State the preparation type.
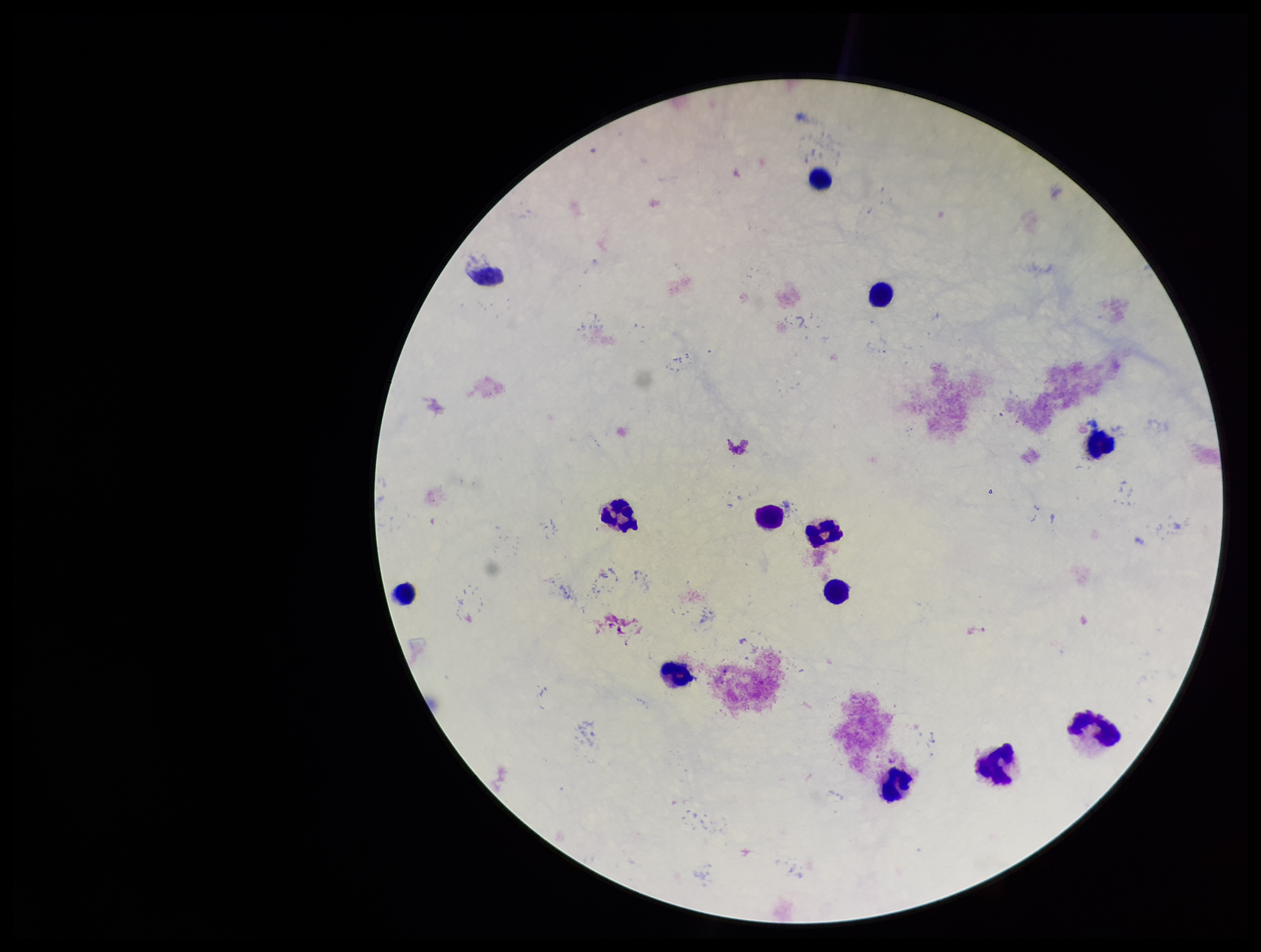
It is a thick blood smear.

Summary:
  - Image size: 1261×952 pixels
  - Field of view: single
  - Leukocyte count: 12
  - Stain: Giemsa
  - Parasite count: 0
  - Capture: smartphone photograph through the microscope eyepiece
  - Plasmodium parasites: none seen
  - Patient malaria status: negative